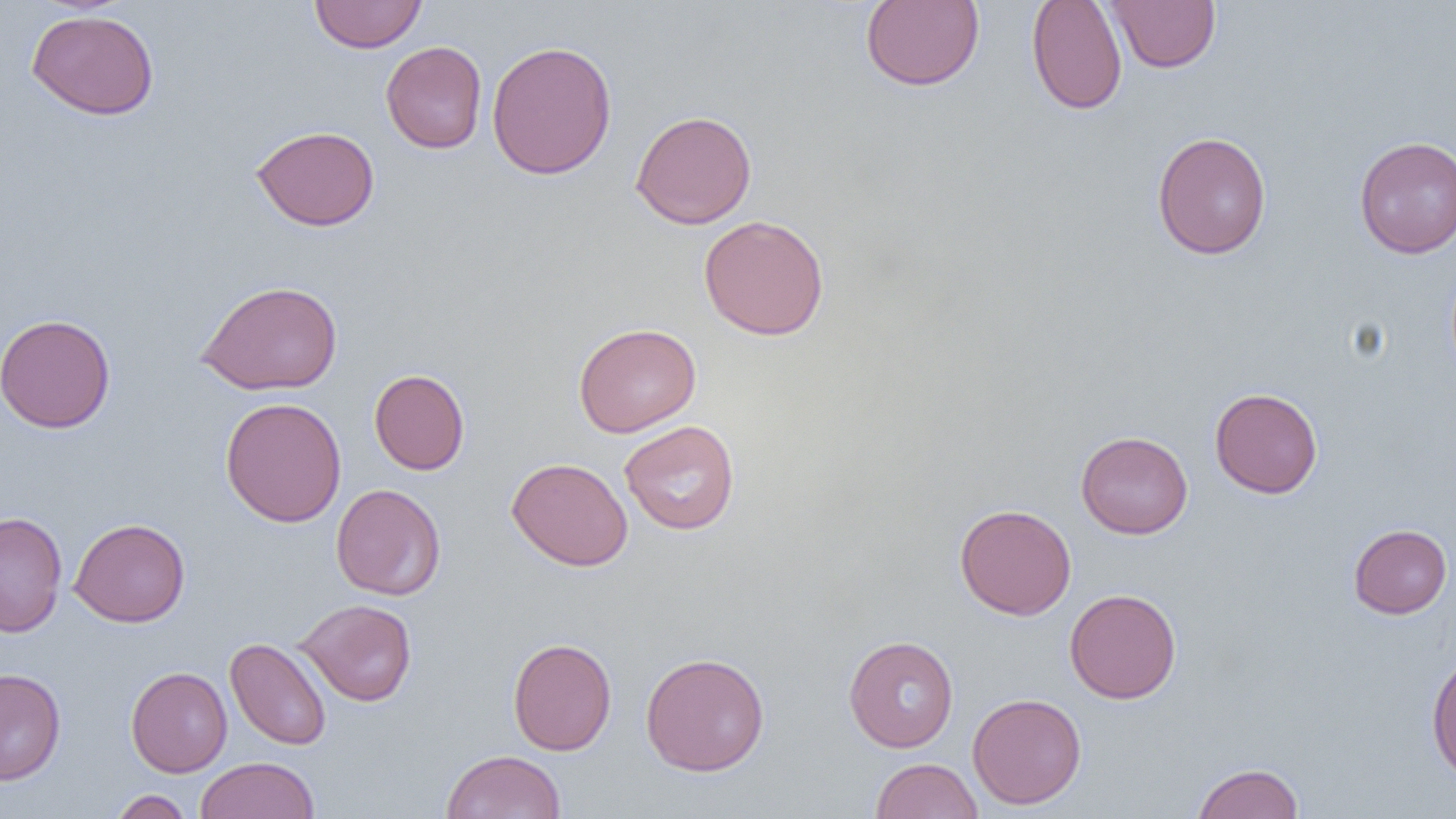
slide-level diagnosis = negative for blood parasites
preparation = thin blood film
field of view = one of a larger specimen
image size = 1456×819 pixels
modality = light microscopy
uninfected red blood cell locations = approximate bounding boxes as (x1,y1)-(x2,y2) corner pairs in pixels: (309,0)-(428,53), (860,0)-(985,91), (1026,0)-(1128,115), (1105,1)-(1221,72), (26,9)-(159,120), (486,40)-(618,181), (381,41)-(487,153), (630,109)-(757,230), (250,125)-(380,231), (1151,131)-(1272,260), (1354,135)-(1456,258), (698,214)-(830,341), (195,279)-(343,395), (0,313)-(116,433), (573,322)-(701,437), (369,369)-(470,475), (1209,387)-(1323,499), (220,396)-(346,527), (619,420)-(740,536), (1076,431)-(1193,539), (507,457)-(633,571), (331,483)-(446,600), (954,504)-(1076,620), (0,511)-(68,636), (69,518)-(190,627), (1348,523)-(1452,619), (1064,588)-(1182,704), (295,599)-(417,706), (843,635)-(959,752), (225,637)-(332,751), (508,637)-(617,755), (1426,649)-(1456,782), (640,651)-(770,777), (126,666)-(232,777), (0,668)-(66,785), (967,692)-(1087,810), (441,749)-(566,819), (196,756)-(320,819), (870,758)-(983,819), (1191,762)-(1304,819), (109,789)-(194,819)
magnification = 1000x